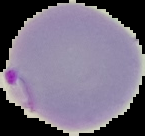
The area outside the segmented cell region is set to black. Result: malaria parasites identified. Image is 145×136 pixels. From a thin blood film.